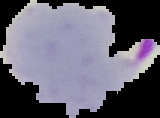
The area outside the segmented cell region is set to black. From a thin blood smear. Result: Plasmodium parasites detected. Image is 160×118 pixels.